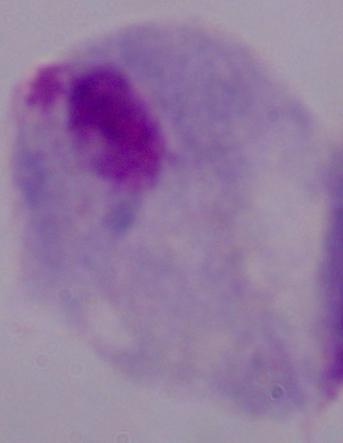

Summary:
  - Magnification: 1000x
  - Modality: photomicrograph
  - Identification: trichomonad